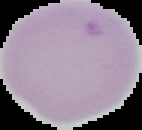
Summary:
  - Malaria status: uninfected
  - Image type: segmented cell region with the area outside set to black
  - Image size: 142×130 pixels
  - Preparation: thin blood smear